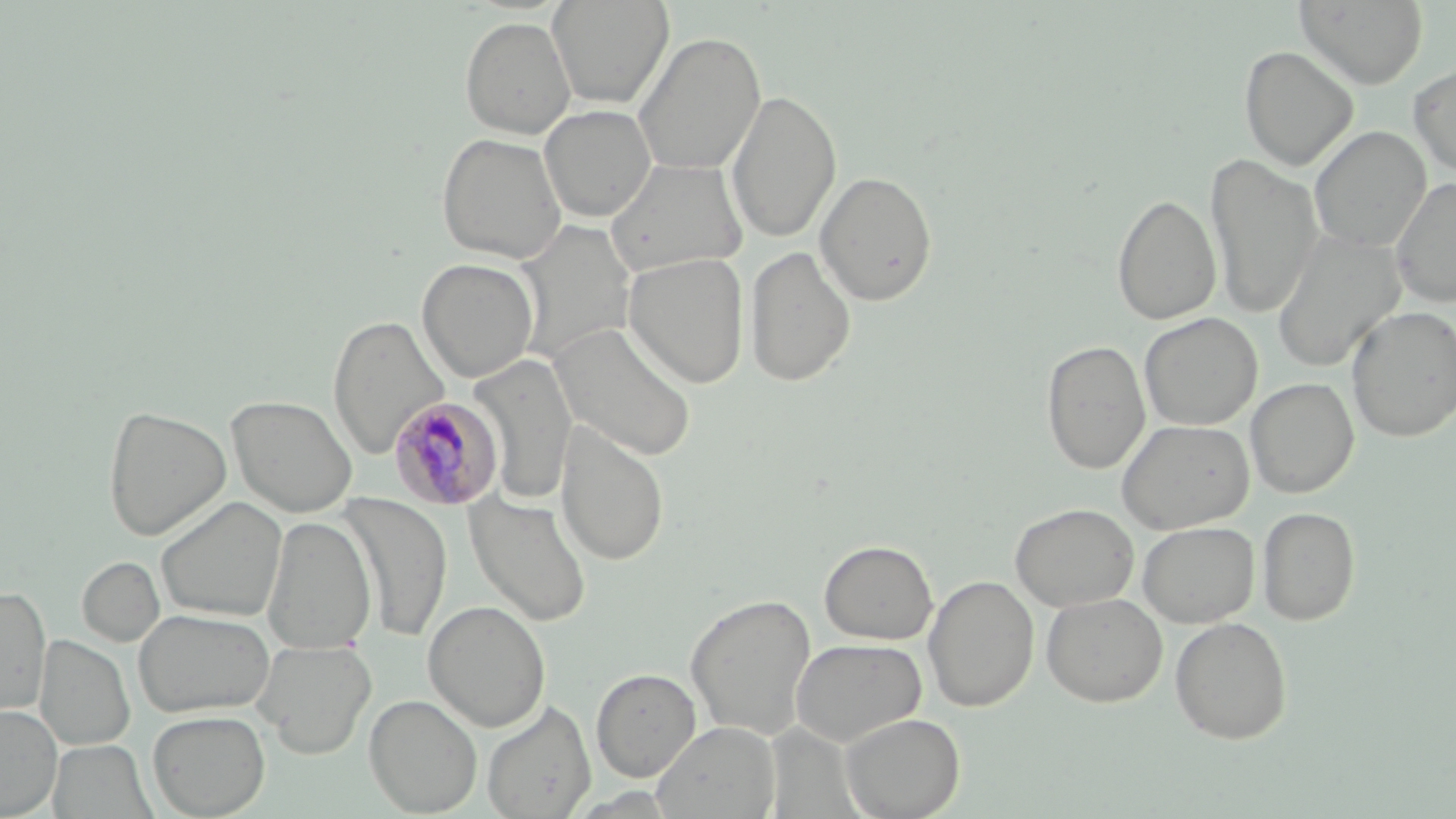
Summary:
  - Coordinate format: approximate bounding boxes as (x1,y1)-(x2,y2) corner pairs in pixels
  - Uninfected red blood cell locations: (547,0)-(674,109), (1293,0)-(1429,89), (459,15)-(576,139), (632,30)-(767,176), (1239,45)-(1358,171), (1409,63)-(1456,179), (726,88)-(841,245), (539,104)-(657,223), (1310,126)-(1432,252), (436,132)-(567,264), (1206,153)-(1323,320), (606,158)-(748,279), (814,171)-(939,306), (1390,176)-(1456,307), (1112,194)-(1221,326), (512,220)-(638,364), (1272,229)-(1405,373), (744,246)-(857,388), (623,251)-(750,389), (416,258)-(540,383), (1347,305)-(1456,442), (1139,313)-(1262,431), (327,314)-(450,460), (550,321)-(696,462), (1041,339)-(1150,475), (469,353)-(578,506), (1246,377)-(1359,499), (226,395)-(358,517), (102,405)-(232,541), (1116,419)-(1254,534), (555,421)-(670,567), (465,491)-(592,627), (339,493)-(454,642), (156,496)-(287,622), (1010,503)-(1139,611), (1257,506)-(1360,625), (262,515)-(377,654), (1138,521)-(1258,627), (819,540)-(938,645), (77,557)-(165,646), (923,575)-(1039,712), (0,586)-(51,719), (1041,592)-(1167,707), (684,593)-(817,740), (423,600)-(551,732), (135,608)-(275,718), (1169,616)-(1292,745), (34,634)-(135,751), (790,637)-(927,748), (253,639)-(377,758), (591,667)-(701,781), (364,694)-(482,816), (481,700)-(596,818), (0,704)-(62,818), (147,710)-(271,818), (839,712)-(965,819), (652,721)-(781,819), (48,740)-(154,818)
  - Plasmodium malariae-infected red blood cell locations: (388,396)-(504,512)
  - Slide-level diagnosis: Plasmodium malariae
  - Modality: light microscopy
  - Stain: May-Grünwald-Giemsa
  - Magnification: 1000x
  - Preparation: thin blood film
  - Field of view: single
  - Image size: 1456×819 pixels